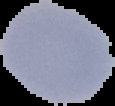
image type = cell region segmented out of the field of view; surrounding area masked to black
result = Plasmodium parasites detected
image size = 115×106 pixels
preparation = thin blood film